State the blood parasite species.
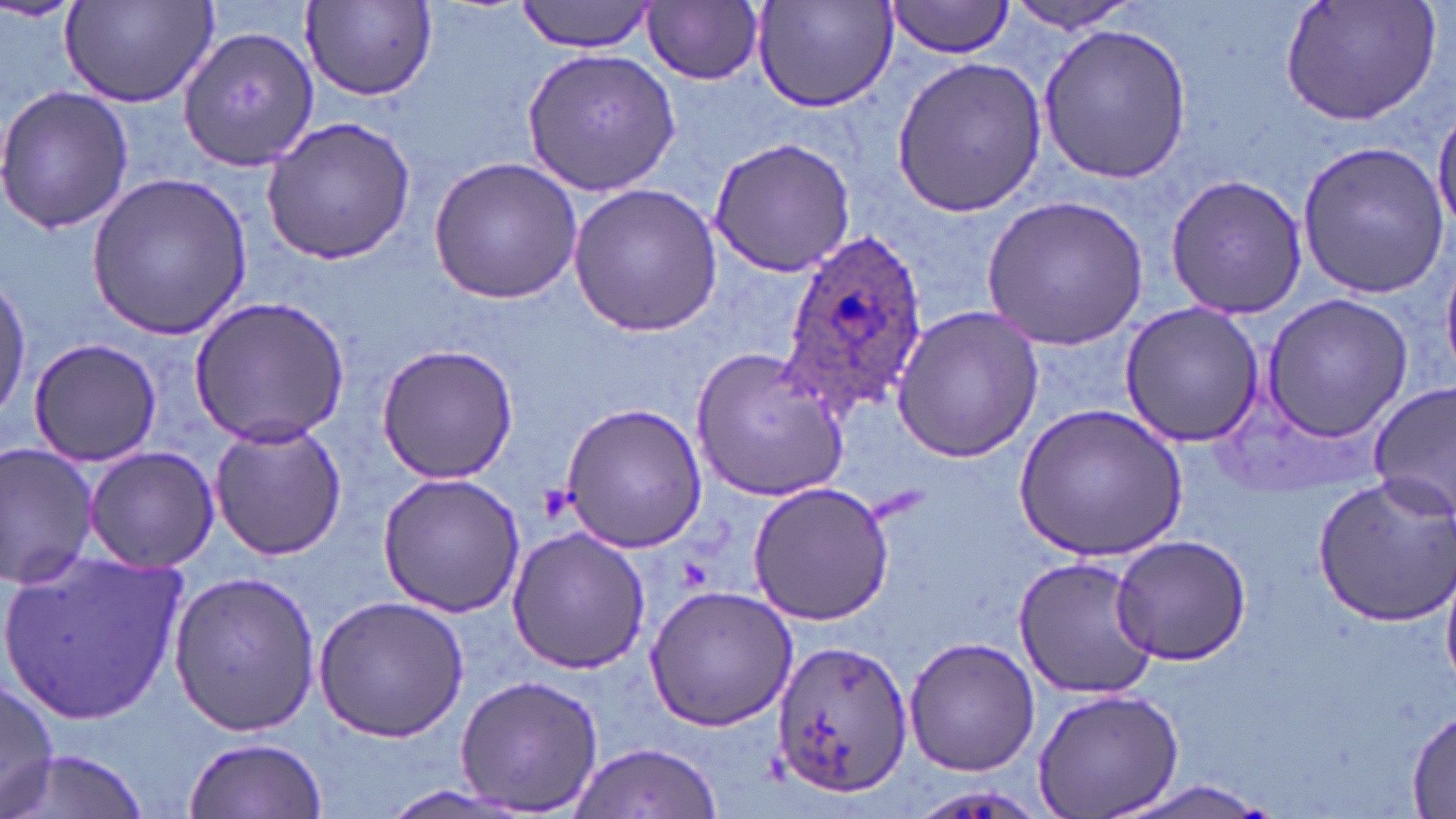

Plasmodium ovale.

Approximate bounding boxes as (x1, y1, x2, y2) in pixels. Uninfected red blood cell locations: (0, 0, 78, 24), (515, 0, 661, 53), (750, 0, 900, 114), (883, 0, 1016, 60), (1279, 0, 1442, 125), (646, 1, 764, 85), (1003, 1, 1147, 34), (58, 2, 217, 109), (302, 2, 436, 100), (1039, 23, 1194, 185), (179, 28, 321, 173), (521, 46, 680, 196), (891, 57, 1049, 217), (0, 86, 134, 235), (1432, 105, 1456, 236), (260, 116, 416, 265), (708, 136, 855, 276), (1296, 141, 1450, 300), (427, 157, 583, 305), (1164, 171, 1308, 321), (84, 172, 256, 338), (565, 183, 725, 337), (981, 193, 1152, 349), (1260, 293, 1415, 441), (190, 295, 350, 446), (1118, 301, 1266, 447), (891, 306, 1044, 463), (29, 336, 159, 467), (375, 343, 519, 484), (692, 344, 849, 503), (1370, 381, 1456, 519), (557, 399, 707, 554), (1016, 402, 1189, 561), (208, 420, 347, 561), (0, 444, 103, 589), (84, 447, 221, 573), (377, 472, 526, 619), (1312, 474, 1456, 627), (746, 481, 894, 627), (506, 525, 652, 674), (1110, 534, 1251, 666), (0, 546, 188, 726), (1013, 557, 1159, 700), (169, 570, 323, 737), (643, 584, 800, 731), (312, 595, 470, 743), (903, 637, 1040, 777), (772, 640, 913, 795), (454, 674, 604, 814), (0, 677, 59, 815), (1031, 687, 1184, 819), (1407, 706, 1456, 814), (185, 736, 328, 818), (568, 741, 725, 818), (10, 750, 149, 819), (1116, 778, 1271, 819). Plasmodium ovale-infected red blood cell locations: (776, 230, 929, 418). Platelet locations: (535, 482, 578, 522), (678, 556, 714, 592). May-Grünwald-Giemsa-stained preparation. Thin blood film. Light microscopy. Single field of view. 1000x magnification. Image is 1456×819 pixels.